Assess this cell for malaria.
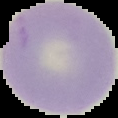
It is uninfected.

From a thin blood film. Image is 118×118 pixels. Segmented cell region on a black background.